Assess this cell for malaria.
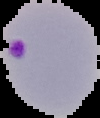
It is parasitized.

preparation = thin blood smear
image type = cell region segmented out of the field of view; surrounding area masked to black
image size = 100×118 pixels